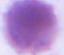
A red blood cell is seen. Photomicrograph. 1000x magnification.